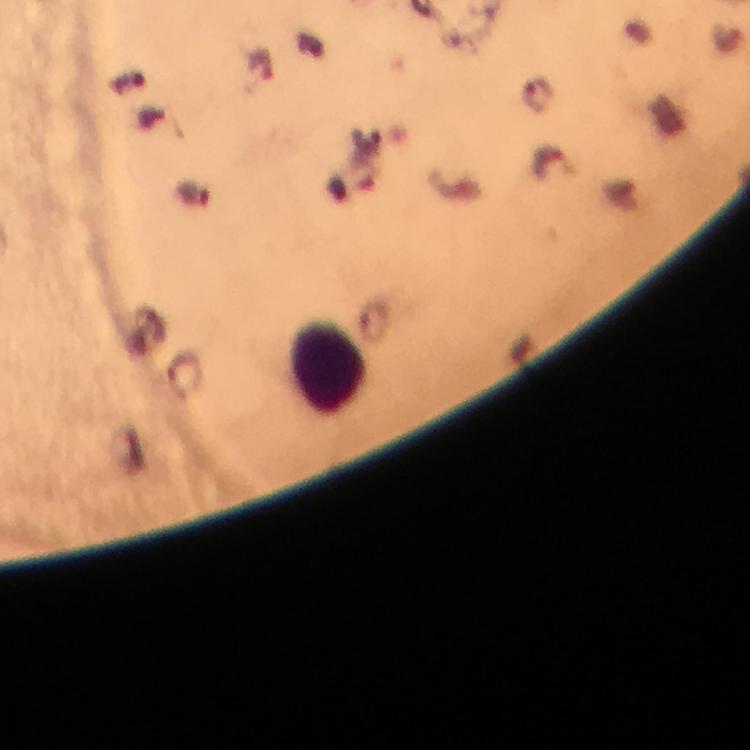

Approximate object centers, in pixels from the top-left corner.
Summary:
  - Leukocyte locations: (x=327, y=367)
  - Plasmodium parasite locations: (x=536, y=93)
  - Stain: Giemsa
  - Magnification: 100x
  - Cropped from: a single field of view
  - Context: from a malaria diagnostic workup
  - Preparation: thick smear
  - Image size: 750×750 pixels
  - Immersion oil: used
  - Capture: smartphone camera through the microscope